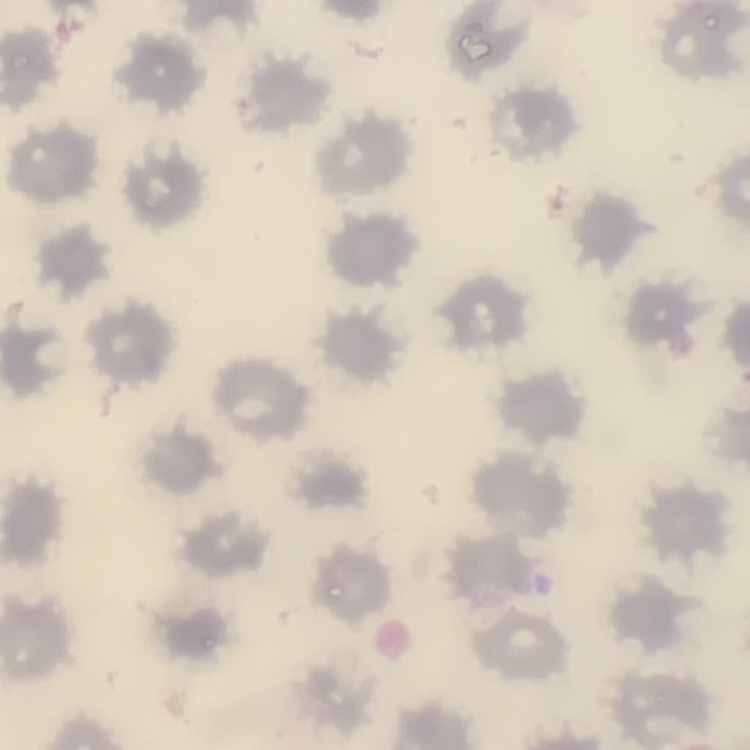

{
  "erythrocyte_morphology": "no rouleaux formation",
  "stain": "Field's or Giemsa",
  "image_type": "one tile cut from a larger photomicrograph",
  "preparation": "thin blood smear"
}